Report the malaria status of this cell.
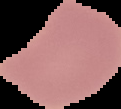

Uninfected.

From a thin blood film. Cell region segmented out of the field of view; the surrounding area is masked to black. Image is 121×109 pixels.